Classify this cell by malaria status.
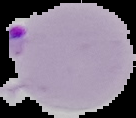

Parasitized.

Cell region segmented out of the field of view; the surrounding area is masked to black. Image is 136×118 pixels. From a thin blood smear.